Identify the parasite.
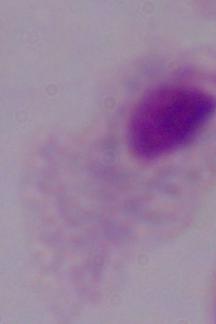
A trichomonad.

magnification = 1000x
modality = micrograph